Comment on the morphology of the red blood cells.
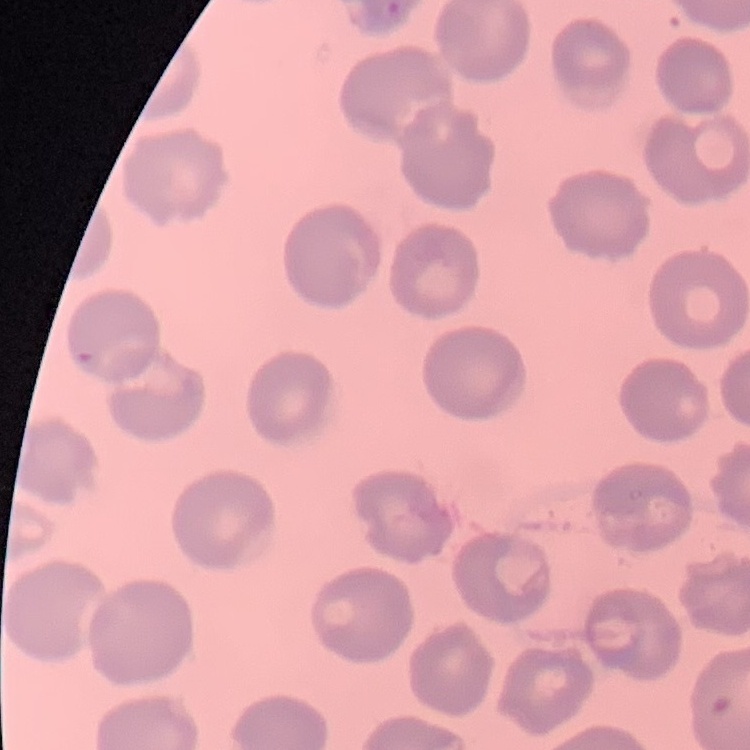

They show no rouleaux formation.

stain = Field's or Giemsa
image type = square crop of a larger photomicrograph
preparation = thin blood smear